Report the malaria status of this cell.
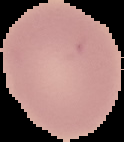
It is uninfected.

Summary:
  - Preparation: thin blood smear
  - Image size: 124×142 pixels
  - Image type: cell region segmented out of the field of view; surrounding area masked to black